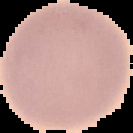
Summary:
  - Image type: cell region segmented out of the field of view; surrounding area masked to black
  - Malaria status: uninfected
  - Image size: 133×133 pixels
  - Preparation: thin blood smear